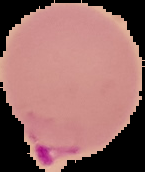

image type = segmented cell region on a black background
preparation = thin blood film
malaria status = parasitized
image size = 145×172 pixels